Mark where platelets are.
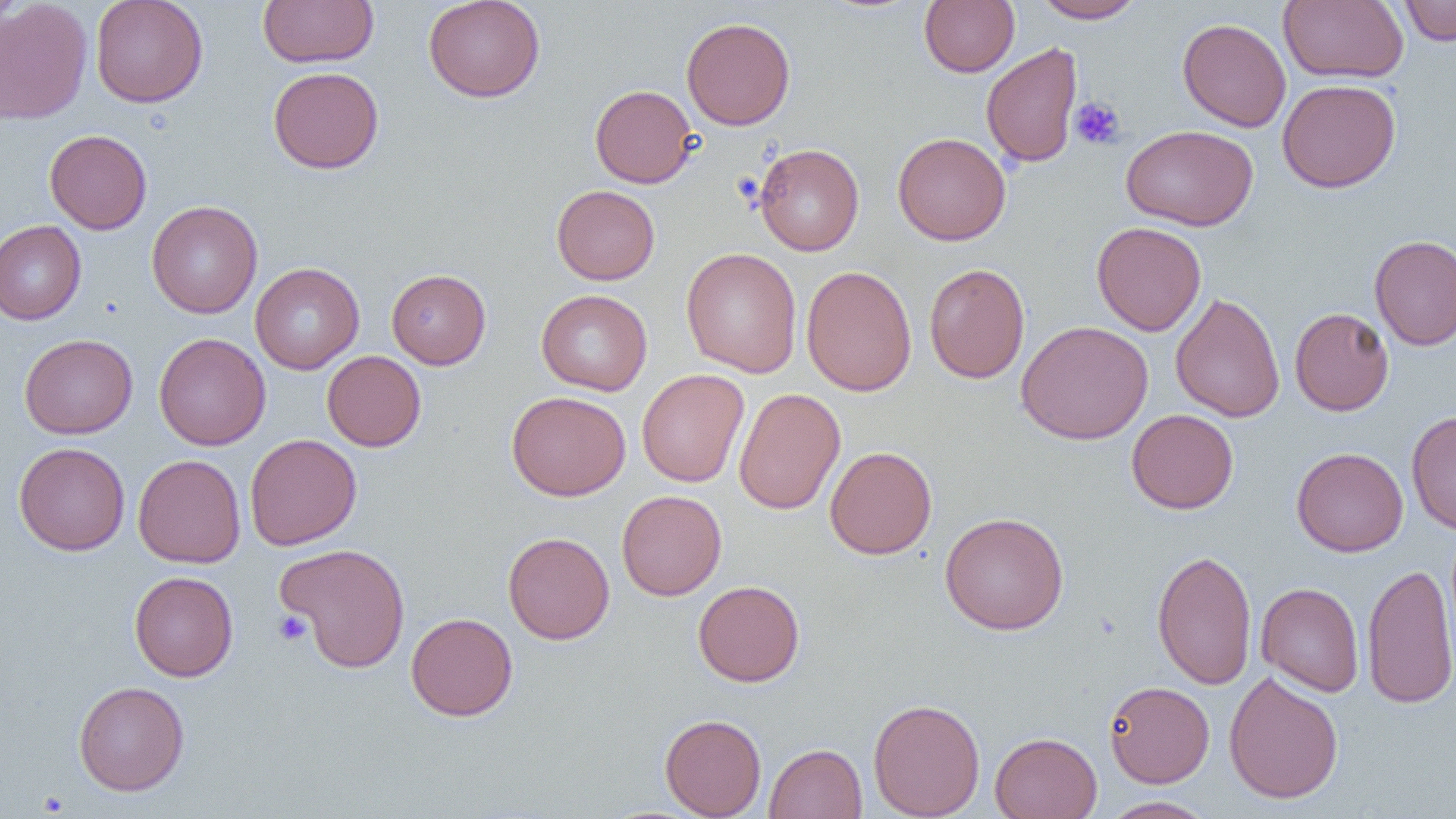

Approximate bounding boxes as (x1, y1, x2, y2) in pixels.
Platelets: (1069, 96, 1126, 151), (273, 610, 313, 646), (36, 790, 70, 816).

Uninfected red blood cell locations: (0, 0, 92, 125), (90, 0, 208, 107), (257, 0, 379, 68), (422, 0, 546, 102), (919, 0, 1019, 77), (1032, 0, 1144, 23), (1278, 0, 1409, 84), (1398, 1, 1456, 46), (681, 17, 796, 130), (1177, 17, 1291, 132), (981, 42, 1082, 169), (268, 67, 384, 174), (1277, 78, 1401, 193), (590, 84, 698, 188), (1121, 125, 1258, 231), (44, 129, 152, 234), (892, 132, 1011, 245), (754, 143, 864, 256), (551, 184, 660, 285), (146, 200, 263, 318), (0, 220, 86, 325), (1092, 221, 1206, 336), (1369, 235, 1456, 350), (681, 247, 802, 378), (250, 262, 364, 374), (924, 263, 1030, 384), (801, 265, 917, 397), (386, 268, 491, 369), (536, 289, 652, 396), (1170, 291, 1285, 423), (1289, 307, 1394, 416), (1015, 320, 1154, 445), (153, 332, 270, 450), (19, 333, 138, 439), (322, 351, 427, 451), (636, 369, 749, 487), (733, 388, 846, 515), (506, 391, 631, 500), (1126, 409, 1239, 514), (1406, 409, 1456, 534), (245, 433, 362, 550), (13, 442, 130, 555), (825, 446, 937, 559), (1291, 447, 1408, 557), (133, 448, 361, 557), (133, 454, 246, 568), (616, 490, 727, 601), (939, 511, 1069, 635), (503, 531, 615, 644), (275, 543, 412, 673), (1152, 549, 1257, 690), (1362, 562, 1456, 709), (129, 571, 238, 681), (693, 580, 805, 687), (1256, 582, 1364, 697), (406, 612, 518, 721), (1224, 670, 1344, 804), (1104, 680, 1214, 787), (73, 681, 189, 796), (868, 697, 985, 818), (660, 714, 766, 818), (989, 731, 1102, 819), (764, 743, 867, 818), (1100, 796, 1215, 818). Slide-level diagnosis: negative for blood parasites. Image is 1456×819 pixels. Captured at 1000x magnification. Thin blood film. One field of a larger specimen. Light microscopy.